Name the blood parasite species.
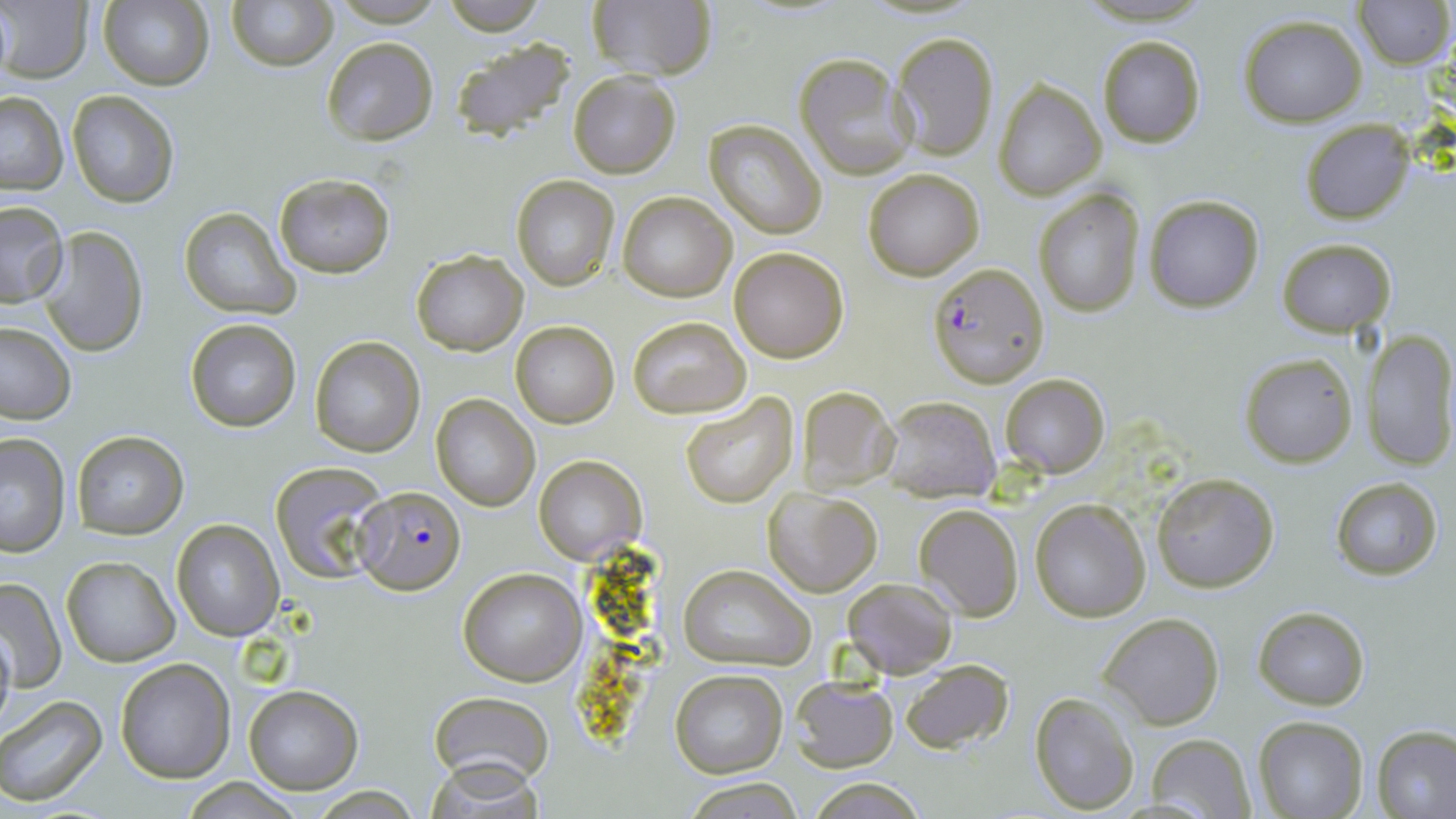
Plasmodium falciparum.

Summary:
  - Coordinate format: approximate bounding boxes as (x1,y1)-(x2,y2) corner pairs in pixels
  - Plasmodium falciparum-infected red blood cell locations: (928,261)-(1048,387), (353,486)-(466,595)
  - Uninfected red blood cell locations: (98,0)-(214,91), (227,0)-(336,71), (443,0)-(547,35), (587,0)-(718,82), (1357,0)-(1452,68), (1,2)-(94,82), (1239,16)-(1367,127), (892,31)-(999,161), (1096,36)-(1206,148), (320,37)-(439,146), (448,37)-(581,145), (794,54)-(914,179), (567,70)-(681,179), (994,80)-(1105,200), (0,92)-(67,194), (67,92)-(178,207), (705,120)-(827,239), (1300,120)-(1414,223), (863,169)-(983,280), (274,174)-(395,277), (511,175)-(620,292), (1032,189)-(1144,317), (618,192)-(737,302), (1145,195)-(1263,313), (0,200)-(70,308), (178,208)-(297,319), (38,225)-(150,358), (1277,237)-(1395,339), (729,246)-(849,363), (411,249)-(528,355), (626,316)-(749,419), (186,318)-(302,433), (510,321)-(619,427), (0,322)-(74,426), (1365,330)-(1456,469), (309,336)-(425,457), (1241,352)-(1358,467), (999,373)-(1110,478), (796,384)-(897,492), (680,392)-(799,510), (429,393)-(540,511), (879,396)-(1000,500), (71,430)-(188,539), (0,433)-(71,557), (533,455)-(647,563), (270,461)-(389,585), (1151,471)-(1280,592), (1330,476)-(1443,582), (764,488)-(883,597), (1029,497)-(1150,622), (914,503)-(1023,620), (172,519)-(284,640), (60,556)-(179,666), (679,565)-(813,670), (456,568)-(587,686), (0,575)-(66,693), (841,577)-(958,677), (1254,606)-(1369,710), (1099,611)-(1224,729), (0,620)-(15,737), (115,658)-(236,784), (896,659)-(1015,754), (669,668)-(788,777), (789,676)-(898,771), (243,684)-(362,795), (1028,691)-(1141,812), (429,692)-(555,783), (0,694)-(107,807), (1253,716)-(1368,819), (1372,725)-(1456,819), (1144,734)-(1258,816), (807,776)-(926,817), (181,778)-(308,816), (682,779)-(807,816)
  - Field of view: one of a larger specimen
  - Magnification: 1000x
  - Stain: May-Grünwald-Giemsa
  - Preparation: thin blood smear
  - Image size: 1456×819 pixels
  - Modality: light microscopy